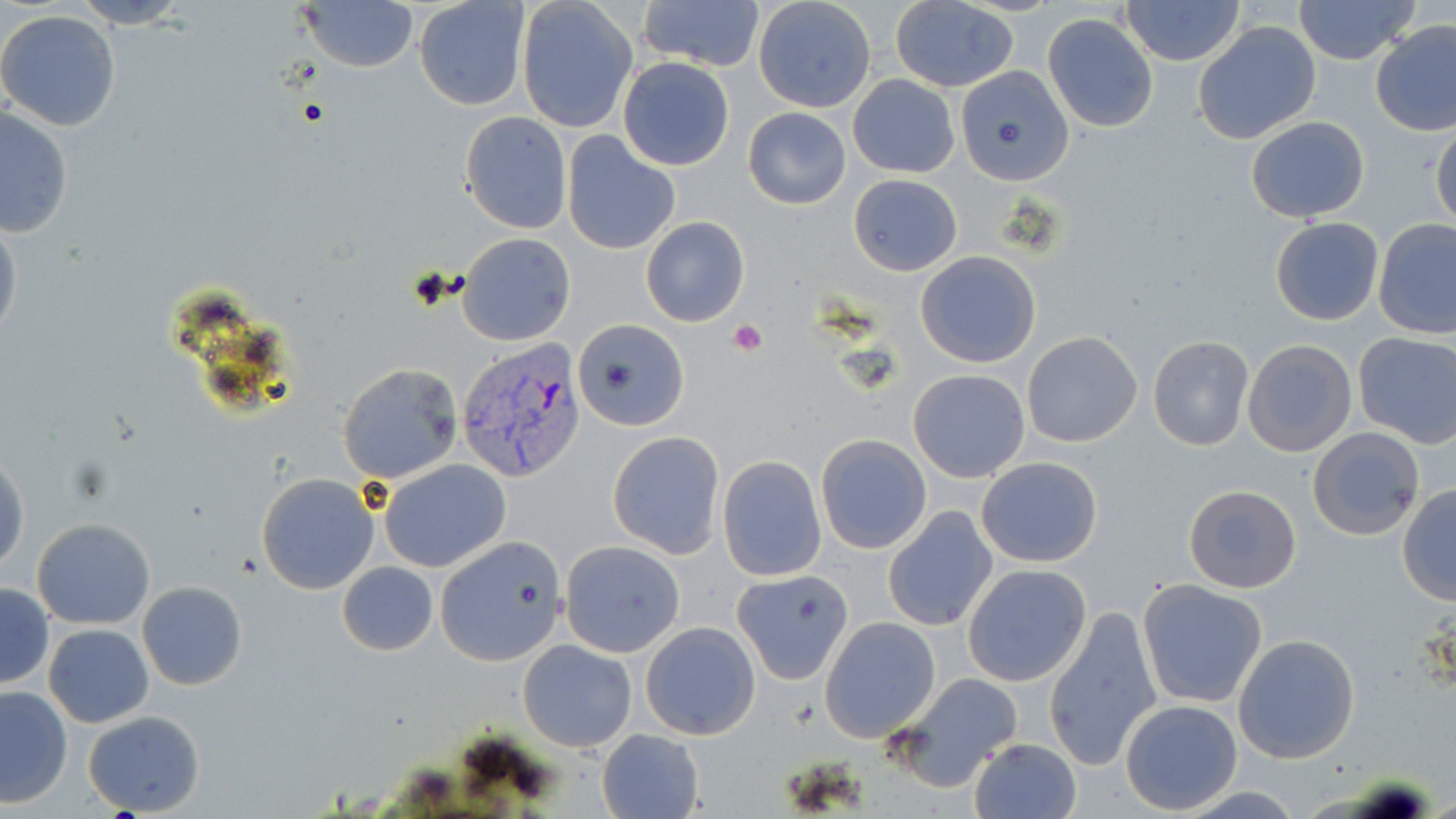

slide_level_diagnosis: Plasmodium vivax
preparation: thin blood film
plasmodium_vivax_infected_red_blood_cell_locations: 'approximate bounding boxes as (x1, y1, x2, y2) in pixels: (456, 338, 587, 482)'
magnification: 1000x
field_of_view: one of a larger specimen
uninfected_red_blood_cell_locations: 'approximate bounding boxes as (x1, y1, x2, y2) in pixels: (71, 0, 193, 28), (414, 0, 529, 111), (638, 0, 765, 73), (1122, 0, 1245, 66), (1293, 0, 1420, 66), (296, 1, 419, 74), (514, 1, 638, 134), (890, 2, 1019, 92), (753, 3, 874, 113), (0, 9, 122, 133), (1043, 12, 1158, 132), (1193, 20, 1322, 144), (1370, 22, 1456, 137), (618, 58, 734, 170), (961, 70, 1077, 192), (847, 75, 960, 178), (1, 107, 74, 239), (743, 108, 851, 209), (459, 111, 572, 234), (1244, 115, 1370, 222), (1431, 118, 1456, 232), (562, 132, 680, 255), (848, 174, 962, 275), (641, 216, 749, 327), (1269, 216, 1384, 326), (0, 219, 22, 343), (1374, 219, 1456, 339), (457, 233, 576, 346), (915, 251, 1042, 369), (573, 320, 688, 431), (1353, 331, 1456, 448), (1022, 332, 1144, 447), (1148, 335, 1253, 452), (1242, 339, 1359, 458), (337, 363, 463, 484), (908, 369, 1030, 484), (1307, 428, 1426, 540), (607, 432, 725, 558), (815, 434, 932, 554), (1, 450, 28, 576), (717, 456, 825, 581), (976, 456, 1103, 567), (377, 458, 512, 573), (257, 473, 379, 593), (1184, 485, 1301, 594), (1397, 485, 1456, 605), (883, 507, 998, 632), (31, 518, 156, 629), (437, 538, 567, 662), (560, 540, 686, 657), (337, 562, 438, 657), (962, 563, 1092, 686), (733, 569, 854, 684), (137, 580, 248, 690), (1136, 580, 1268, 708), (0, 583, 52, 689), (1044, 603, 1162, 772), (819, 617, 941, 741), (640, 621, 761, 741), (43, 623, 154, 728), (1232, 634, 1361, 764), (517, 639, 637, 752), (891, 671, 1024, 793), (1, 686, 73, 808), (1121, 699, 1243, 815), (83, 709, 206, 817), (597, 730, 704, 819), (968, 738, 1083, 819)'
modality: optical microscopy
image_size: 1456×819 pixels
platelet_locations: 'approximate bounding boxes as (x1, y1, x2, y2) in pixels: (729, 319, 768, 357)'
stain: May-Grünwald-Giemsa